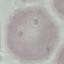

Result: no malaria parasites detected. Photographed with a smartphone camera at the microscope eyepiece. Automatically extracted cell patch, resized to 64 × 64 pixels. Thin blood film. Giemsa stain.